Assess this cell for malaria.
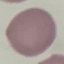

Uninfected.

Summary:
  - Stain: Giemsa
  - Image type: automatically extracted cell patch, resized to 64 × 64 pixels
  - Capture: smartphone camera at the microscope eyepiece
  - Preparation: thin smear